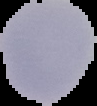

preparation = thin blood film
image size = 97×106 pixels
result = Plasmodium parasites detected
image type = cell region segmented out of the field of view; surrounding area masked to black